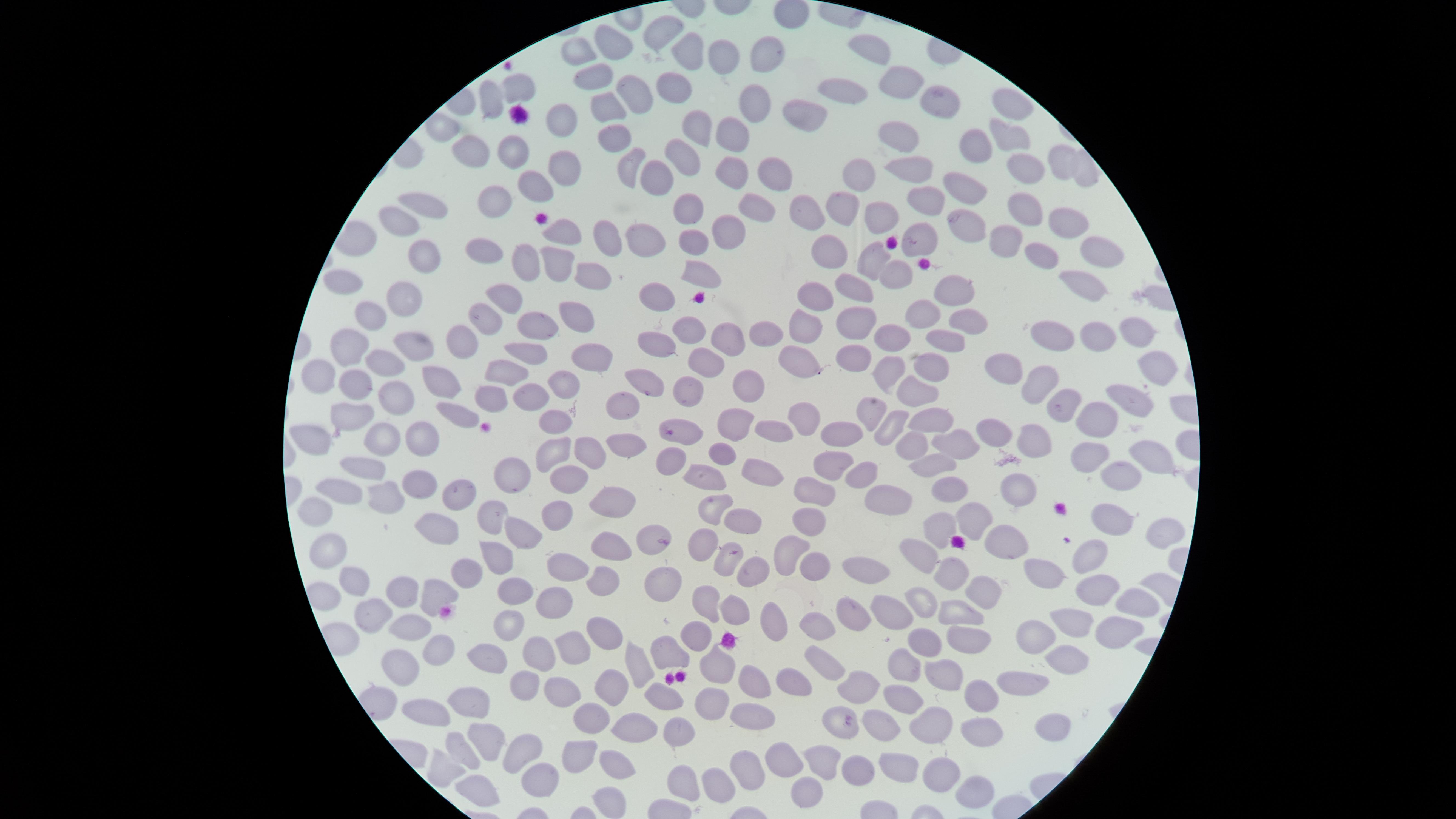

Approximate marker points as [x, y] in pixels.
Summary:
  - Uninfected red blood cells: [662, 26], [618, 41], [870, 46], [582, 47], [726, 49], [690, 53], [763, 63], [595, 79], [675, 81], [900, 82], [513, 84], [632, 92], [847, 96], [484, 101], [755, 102], [605, 106], [1014, 106], [944, 107], [802, 111], [560, 119], [695, 125], [1007, 131], [897, 133], [733, 137], [617, 138], [977, 145], [464, 150], [510, 151], [683, 161], [566, 162], [1060, 162], [1023, 166], [628, 168], [910, 168], [783, 169], [735, 173], [658, 178], [855, 179], [535, 187], [968, 189], [494, 200], [423, 201], [922, 201], [685, 203], [1024, 205], [847, 206], [765, 215], [809, 216], [885, 217], [1065, 219], [398, 221], [969, 221], [561, 230], [727, 233], [609, 236], [1007, 236], [919, 239], [646, 244], [691, 245], [485, 247], [832, 247], [1088, 247], [1038, 253], [421, 257], [521, 260], [557, 261], [873, 265], [592, 273], [702, 274], [900, 274], [340, 281], [1088, 283], [951, 285], [859, 289], [654, 295], [813, 298], [401, 300], [504, 302], [574, 312], [928, 316], [961, 316], [369, 317], [486, 317], [534, 322], [693, 322], [856, 322], [761, 327], [809, 330], [891, 332], [1135, 334], [725, 338], [946, 338], [1041, 339], [1096, 339], [341, 342], [413, 342], [461, 343], [654, 349], [525, 353], [852, 354], [592, 359], [708, 361], [808, 361], [381, 366], [1005, 366], [1159, 370], [325, 372], [504, 372], [887, 372], [934, 372], [358, 379], [438, 380], [1038, 383], [566, 384], [649, 387], [753, 387], [915, 391], [684, 394], [529, 396], [394, 397], [1130, 397], [619, 398], [487, 400], [1065, 403], [1102, 408], [348, 412], [453, 415], [870, 417], [932, 417], [807, 418], [559, 425], [741, 425], [894, 426], [846, 429], [687, 432], [772, 432], [996, 432], [312, 434], [385, 437], [1036, 437], [418, 439], [626, 442], [955, 443], [910, 445], [550, 448], [593, 449], [1090, 453], [1147, 453], [725, 456], [926, 463], [361, 464], [834, 465], [758, 472], [566, 473], [863, 474], [705, 475], [510, 478], [1118, 478], [335, 484], [417, 484], [1015, 487], [942, 488], [812, 493], [456, 495], [609, 501], [314, 503], [382, 503], [713, 507], [885, 507], [559, 512], [491, 516], [746, 517], [1104, 518], [967, 520], [435, 528], [809, 528], [518, 530], [941, 531], [1160, 536], [643, 545], [609, 547], [701, 548], [999, 548], [1091, 548], [335, 549], [788, 550], [498, 556], [919, 557], [729, 563], [866, 563], [811, 564], [561, 571], [752, 571], [1042, 578], [460, 579], [947, 579], [1088, 586], [358, 588], [601, 588], [655, 589], [519, 595], [976, 595], [400, 596], [433, 596], [921, 600], [1125, 600], [705, 603], [550, 606], [734, 611], [889, 611], [957, 612], [370, 617], [852, 618], [776, 621], [1066, 622], [818, 623], [408, 628], [506, 628], [602, 629], [1108, 633], [962, 634], [1038, 636], [701, 637], [920, 639], [576, 644], [433, 651], [536, 654], [493, 656], [1064, 658], [829, 661], [402, 665], [901, 666], [717, 667], [634, 669], [941, 669], [751, 675], [786, 680], [522, 682], [1022, 684], [608, 686], [561, 687], [858, 691], [657, 698], [713, 699], [904, 700], [990, 700], [466, 704], [437, 714], [755, 716], [590, 722], [839, 723], [632, 725], [931, 726], [1050, 728], [685, 730], [981, 730], [883, 732], [487, 737], [457, 747], [525, 747], [576, 752], [822, 754], [786, 758], [621, 764], [896, 765], [444, 769], [751, 769], [859, 771], [676, 776], [539, 778], [942, 778], [717, 781], [807, 786], [974, 791]
  - Visible region: circular
  - Field of view: single
  - Stain: Giemsa
  - Capture: smartphone photograph through the microscope eyepiece
  - Preparation: thin smear of blood
  - Image size: 1456×819 pixels
  - Presence: no malaria parasites identified